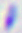

modality = micrograph
identification = Toxoplasma gondii
magnification = 400x